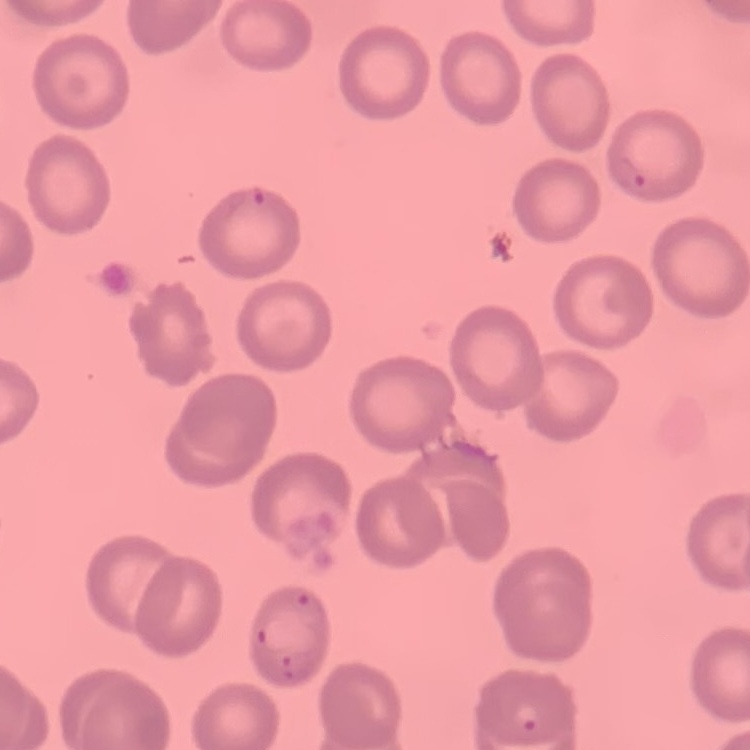 The erythrocytes exhibit no rouleaux formation. Square crop of a larger photomicrograph. Thin blood smear. Stained with either Field's or Giemsa.